Identify the parasite.
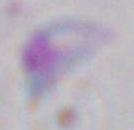

Toxoplasma gondii.

{
  "modality": "micrograph",
  "magnification": "1000x"
}